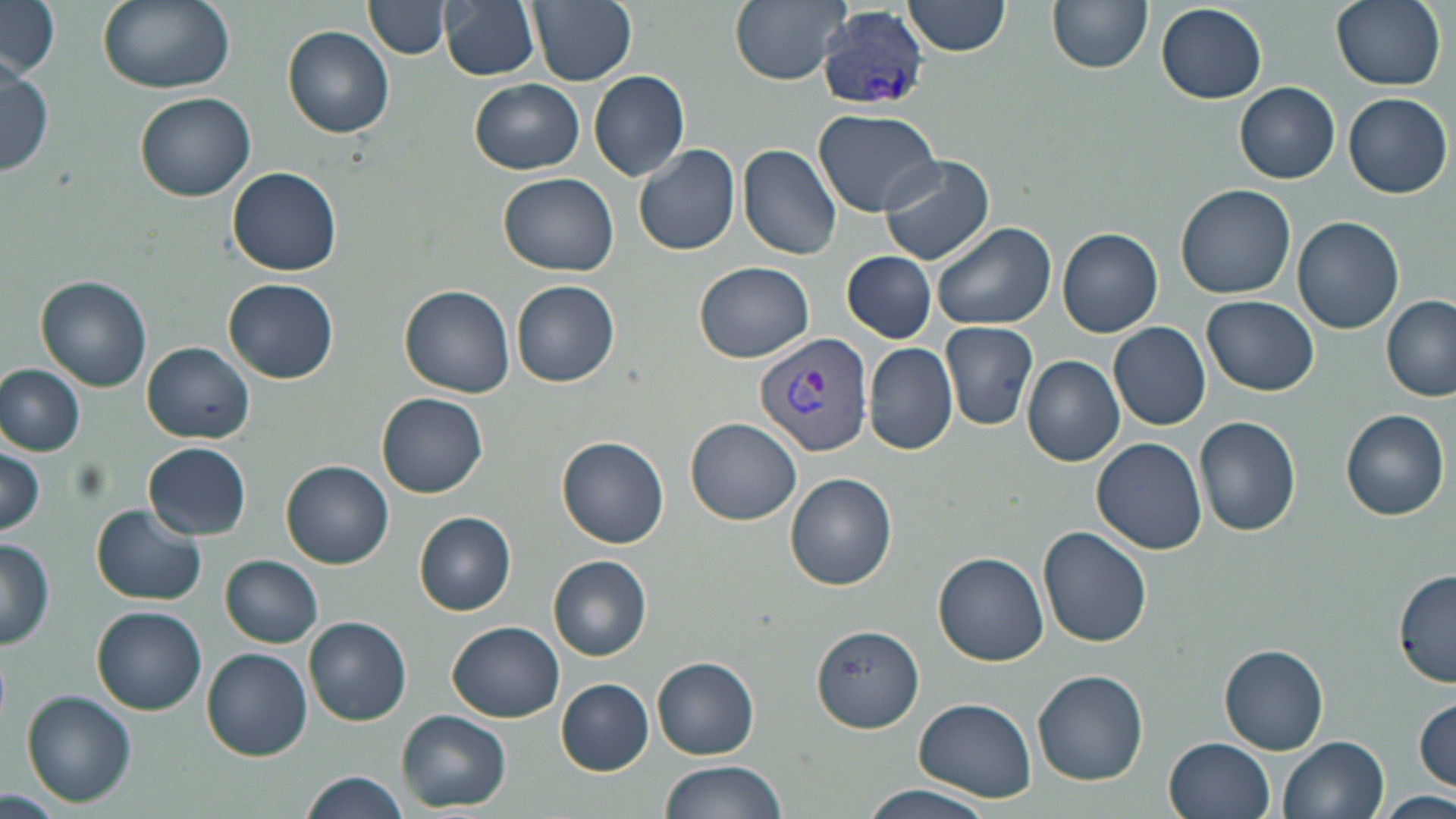
Approximate bounding boxes as (x1, y1, x2, y2) in pixels. Plasmodium vivax-infected red blood cell locations: (816, 8, 930, 111), (755, 331, 875, 458). Uninfected red blood cell locations: (1, 0, 61, 78), (97, 0, 235, 93), (365, 0, 449, 59), (439, 0, 540, 80), (528, 0, 637, 85), (729, 0, 851, 85), (902, 0, 1011, 58), (1046, 0, 1154, 74), (1331, 0, 1448, 90), (1155, 4, 1265, 103), (284, 26, 393, 139), (0, 54, 53, 178), (590, 70, 690, 180), (470, 78, 585, 174), (1234, 81, 1340, 182), (135, 92, 255, 202), (1342, 92, 1453, 198), (815, 110, 943, 218), (635, 144, 740, 255), (739, 144, 842, 259), (877, 154, 994, 265), (228, 167, 341, 276), (498, 172, 620, 273), (1176, 182, 1296, 298), (1292, 216, 1404, 334), (930, 221, 1056, 330), (1058, 228, 1162, 337), (842, 251, 936, 342), (695, 261, 814, 360), (37, 277, 152, 391), (224, 278, 339, 383), (512, 281, 620, 388), (401, 286, 515, 398), (1382, 294, 1455, 401), (1203, 295, 1318, 395), (942, 321, 1040, 428), (1108, 322, 1210, 430), (865, 342, 957, 456), (143, 343, 254, 443), (1023, 355, 1125, 466), (0, 365, 86, 455), (378, 393, 488, 498), (1341, 409, 1448, 520), (1194, 416, 1301, 536), (684, 417, 801, 525), (558, 436, 669, 547), (1091, 437, 1209, 554), (144, 441, 251, 539), (0, 445, 46, 538), (281, 459, 394, 568), (785, 473, 898, 590), (90, 505, 207, 607), (415, 511, 517, 615), (1038, 525, 1152, 648), (0, 538, 55, 650), (934, 549, 1049, 666), (221, 554, 324, 647), (549, 556, 652, 660), (1394, 569, 1456, 688), (92, 606, 206, 714), (304, 616, 412, 725), (447, 620, 564, 721), (811, 623, 926, 732), (1221, 646, 1330, 754), (202, 647, 313, 760), (652, 654, 760, 760), (1033, 669, 1148, 785), (556, 679, 653, 774), (22, 691, 135, 805), (915, 697, 1038, 800), (1414, 697, 1455, 791), (399, 710, 511, 812), (1279, 735, 1388, 818), (1164, 736, 1276, 819), (658, 760, 788, 819), (298, 769, 410, 819), (0, 784, 64, 814), (854, 784, 999, 819), (1380, 790, 1456, 818). Slide-level diagnosis: Plasmodium vivax. One field of a larger specimen. Image is 1456×819 pixels. May-Grünwald-Giemsa-stained preparation. Captured at 1000x magnification. Light microscopy. Thin blood film.